Classify this cell by malaria status.
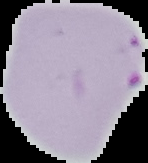

Parasitized.

Cell region segmented out of the field of view; the surrounding area is masked to black. Image is 148×163 pixels. From a thin blood smear.